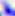

Summary:
  - Magnification: 400x
  - Identification: Toxoplasma gondii
  - Modality: micrograph